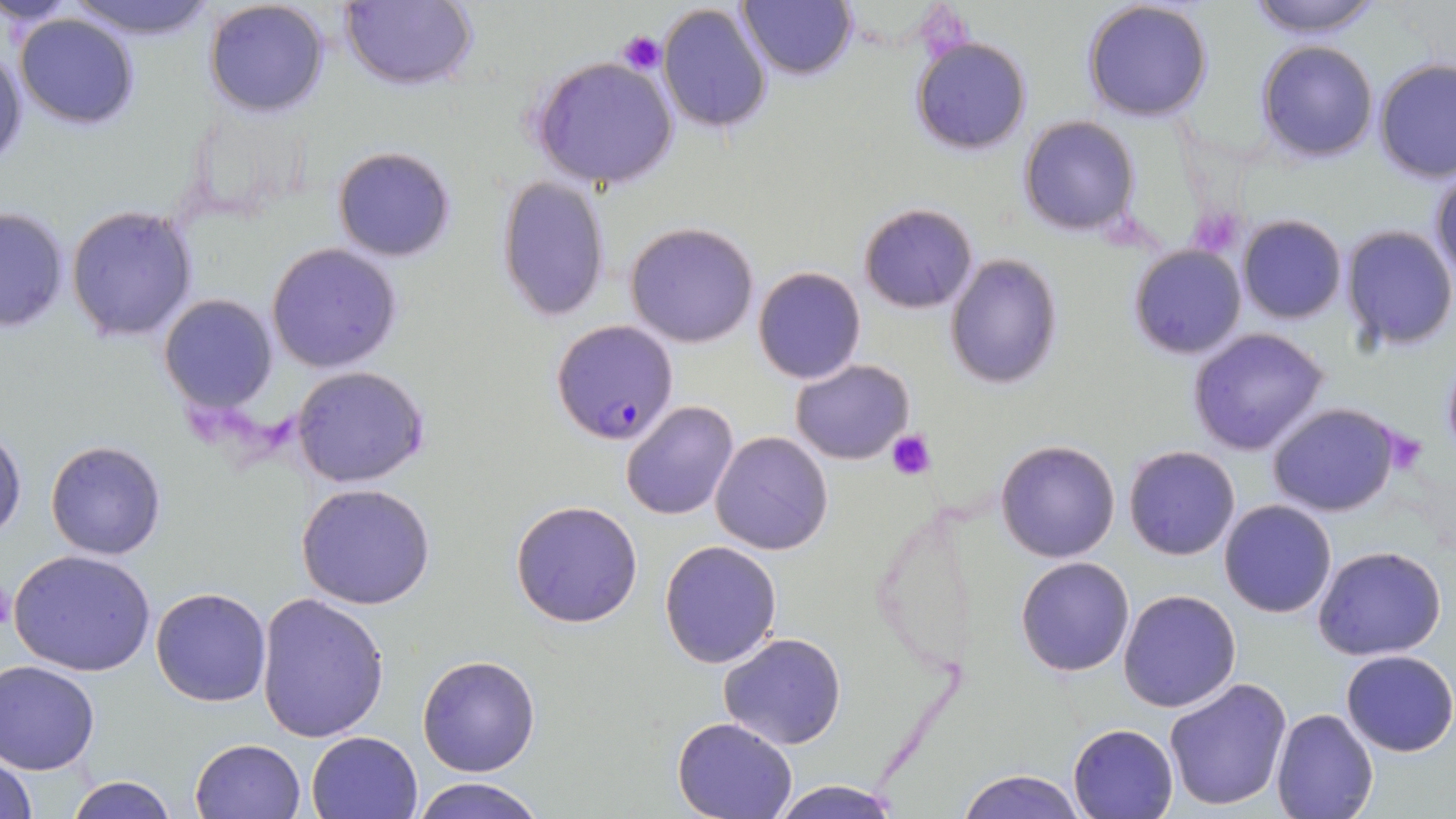
slide-level diagnosis = Plasmodium falciparum
uninfected red blood cell locations = approximate bounding boxes as named x1/y1/x2/y2 corners in pixels: (x1=60, y1=0, x2=222, y2=40), (x1=341, y1=0, x2=480, y2=90), (x1=737, y1=0, x2=856, y2=80), (x1=1081, y1=0, x2=1215, y2=123), (x1=1243, y1=0, x2=1387, y2=39), (x1=203, y1=1, x2=332, y2=117), (x1=658, y1=3, x2=774, y2=135), (x1=13, y1=11, x2=142, y2=129), (x1=909, y1=34, x2=1033, y2=155), (x1=0, y1=39, x2=27, y2=170), (x1=1257, y1=41, x2=1378, y2=163), (x1=529, y1=55, x2=681, y2=189), (x1=1374, y1=60, x2=1456, y2=185), (x1=1019, y1=116, x2=1141, y2=237), (x1=331, y1=145, x2=457, y2=263), (x1=1429, y1=169, x2=1456, y2=288), (x1=497, y1=177, x2=611, y2=323), (x1=0, y1=204, x2=71, y2=334), (x1=67, y1=204, x2=199, y2=343), (x1=859, y1=204, x2=978, y2=313), (x1=1237, y1=214, x2=1347, y2=324), (x1=625, y1=222, x2=759, y2=348), (x1=1338, y1=225, x2=1455, y2=353), (x1=266, y1=242, x2=403, y2=373), (x1=1127, y1=244, x2=1246, y2=359), (x1=945, y1=254, x2=1062, y2=390), (x1=753, y1=266, x2=866, y2=385), (x1=158, y1=294, x2=279, y2=414), (x1=1186, y1=326, x2=1331, y2=456), (x1=791, y1=358, x2=915, y2=465), (x1=290, y1=365, x2=431, y2=489), (x1=620, y1=401, x2=741, y2=520), (x1=1265, y1=402, x2=1403, y2=517), (x1=0, y1=419, x2=26, y2=545), (x1=710, y1=431, x2=834, y2=555), (x1=43, y1=438, x2=168, y2=560), (x1=995, y1=439, x2=1121, y2=562), (x1=1124, y1=444, x2=1241, y2=561), (x1=296, y1=483, x2=438, y2=611), (x1=510, y1=499, x2=644, y2=629), (x1=1219, y1=501, x2=1337, y2=619), (x1=659, y1=539, x2=782, y2=668), (x1=1313, y1=546, x2=1447, y2=662), (x1=9, y1=549, x2=157, y2=678), (x1=1015, y1=556, x2=1136, y2=677), (x1=150, y1=586, x2=272, y2=707), (x1=1117, y1=589, x2=1242, y2=714), (x1=256, y1=593, x2=391, y2=745), (x1=719, y1=633, x2=846, y2=750), (x1=1341, y1=649, x2=1456, y2=757), (x1=417, y1=654, x2=541, y2=775), (x1=0, y1=659, x2=101, y2=774), (x1=1163, y1=677, x2=1295, y2=812), (x1=1271, y1=708, x2=1378, y2=819), (x1=671, y1=716, x2=800, y2=819), (x1=1068, y1=722, x2=1180, y2=818), (x1=306, y1=729, x2=424, y2=819), (x1=190, y1=738, x2=307, y2=819), (x1=1, y1=749, x2=37, y2=819), (x1=957, y1=768, x2=1087, y2=819), (x1=64, y1=774, x2=180, y2=819), (x1=410, y1=776, x2=549, y2=819), (x1=764, y1=779, x2=905, y2=818)
image size = 1456×819 pixels
modality = optical microscopy
preparation = thin blood film
field of view = one of a larger specimen
Plasmodium falciparum-infected red blood cell locations = approximate bounding boxes as named x1/y1/x2/y2 corners in pixels: (x1=550, y1=318, x2=679, y2=447)
platelet locations = approximate bounding boxes as named x1/y1/x2/y2 corners in pixels: (x1=618, y1=30, x2=667, y2=74), (x1=887, y1=431, x2=934, y2=480)
stain = May-Grünwald-Giemsa
magnification = 1000x